Comment on the morphology of the erythrocytes.
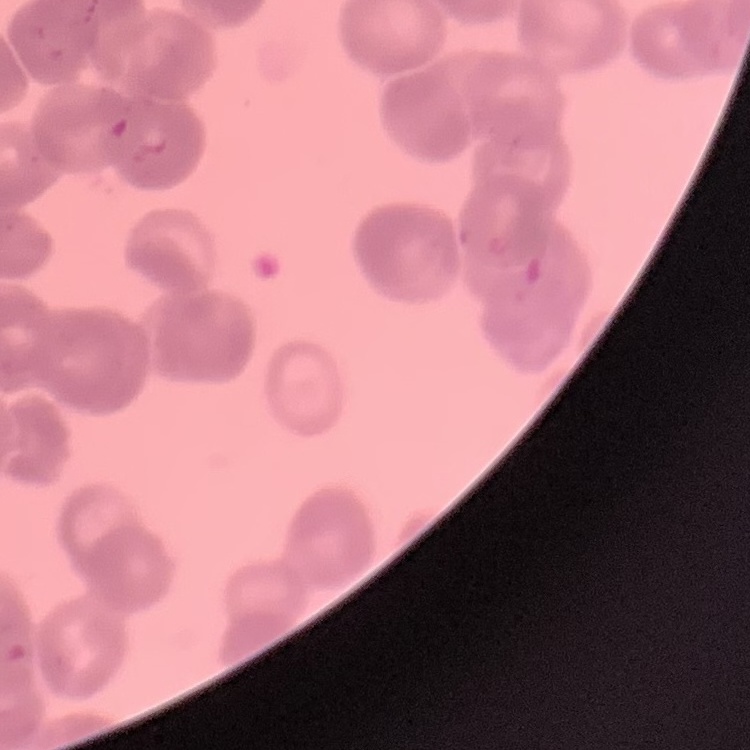
Rouleaux formation.

stain = Field's or Giemsa
image type = one tile cut from a larger photomicrograph
preparation = thin blood film